Locate every malaria parasite and every leukocyte.
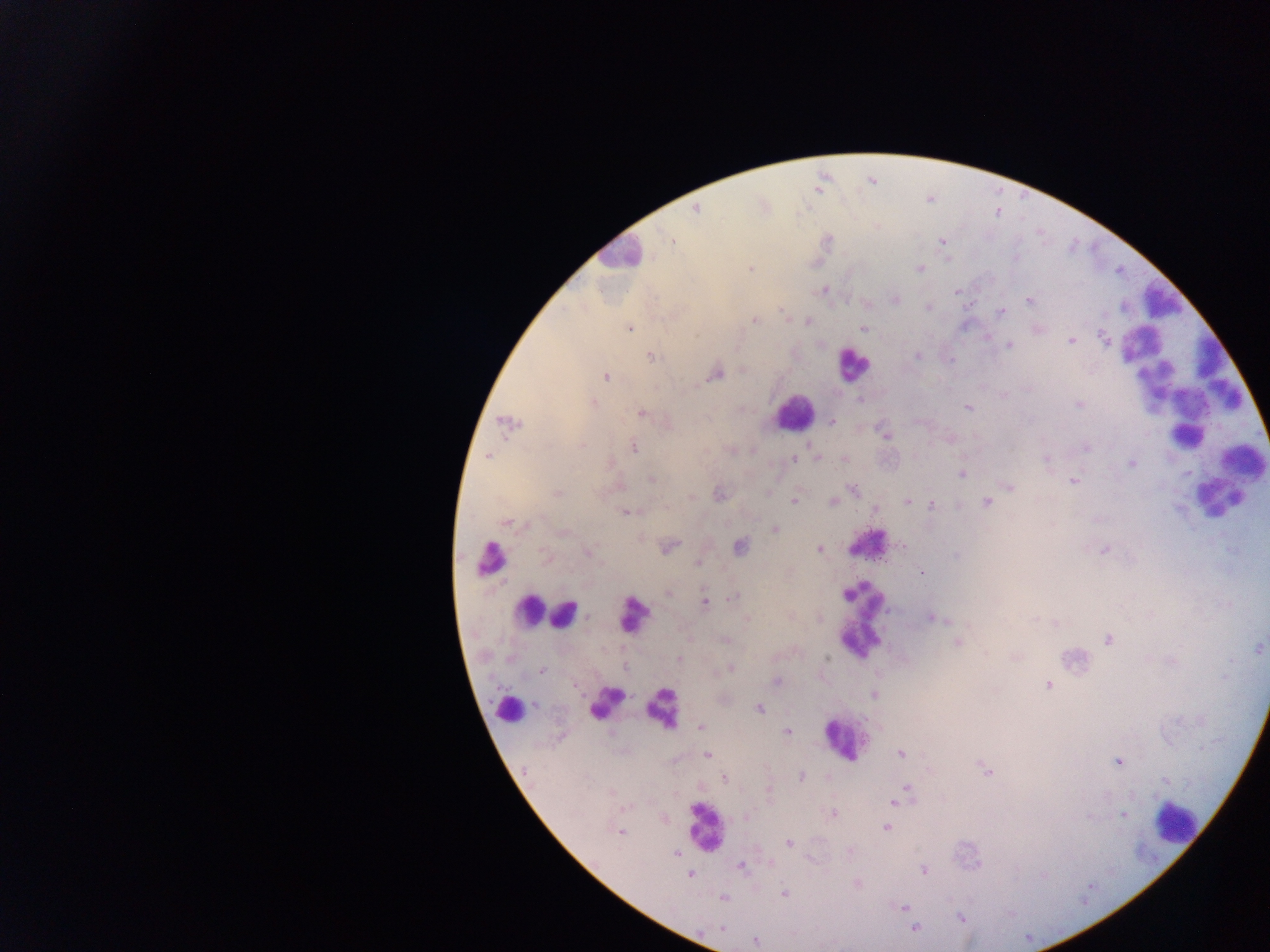

Approximate centers as {x, y} in pixels.
Malaria parasites: {870, 181}, {820, 184}, {696, 209}, {669, 241}, {942, 241}, {750, 269}, {919, 269}, {823, 290}, {957, 291}, {895, 299}, {1029, 299}, {970, 304}, {928, 306}, {1001, 313}, {786, 319}, {754, 320}, {807, 321}, {628, 327}, {863, 327}, {1037, 329}, {987, 338}, {1104, 339}, {1072, 340}, {1008, 345}, {917, 355}, {650, 357}, {714, 373}, {606, 376}, {1003, 394}, {860, 399}, {593, 403}, {1080, 404}, {966, 407}, {640, 413}, {830, 421}, {506, 423}, {885, 434}, {950, 439}, {633, 447}, {1085, 447}, {488, 456}, {818, 458}, {844, 458}, {1047, 458}, {795, 459}, {1131, 463}, {961, 473}, {651, 479}, {1074, 480}, {617, 486}, {1010, 486}, {853, 489}, {557, 493}, {719, 494}, {692, 497}, {794, 500}, {986, 501}, {831, 502}, {906, 502}, {958, 504}, {931, 505}, {874, 508}, {627, 511}, {506, 522}, {775, 529}, {740, 546}, {902, 546}, {667, 547}, {819, 549}, {1105, 549}, {588, 551}, {544, 556}, {698, 562}, {922, 573}, {669, 591}, {729, 598}, {704, 602}, {931, 616}, {1108, 638}, {725, 640}, {957, 642}, {1259, 647}, {1015, 656}, {679, 660}, {730, 668}, {541, 669}, {775, 681}, {573, 682}, {1049, 685}, {873, 694}, {758, 708}, {701, 726}, {787, 732}, {900, 754}, {707, 755}, {1117, 761}, {987, 772}, {801, 776}, {724, 778}, {1164, 781}, {906, 787}, {893, 803}, {834, 813}, {1122, 814}, {886, 828}, {619, 831}, {789, 843}, {850, 851}, {677, 853}, {771, 862}, {740, 865}, {924, 869}, {690, 873}, {856, 883}, {783, 893}, {723, 897}, {903, 907}, {914, 927}, {756, 940}.
Leukocytes: {619, 255}, {1162, 300}, {853, 363}, {794, 414}, {1185, 435}, {1242, 461}, {1219, 498}, {867, 543}, {489, 559}, {529, 609}, {564, 613}, {632, 614}, {859, 620}, {605, 702}, {662, 708}, {509, 709}, {845, 738}, {1173, 820}, {704, 828}.

Thick blood film. Image is 1270×952 pixels. Mobile-phone photograph taken through the microscope. Sample from Ghana. One field of view.